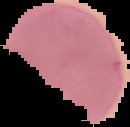

From a thin blood smear. Segmented cell region on a black background. Image is 130×127 pixels. Result: malaria parasites identified.